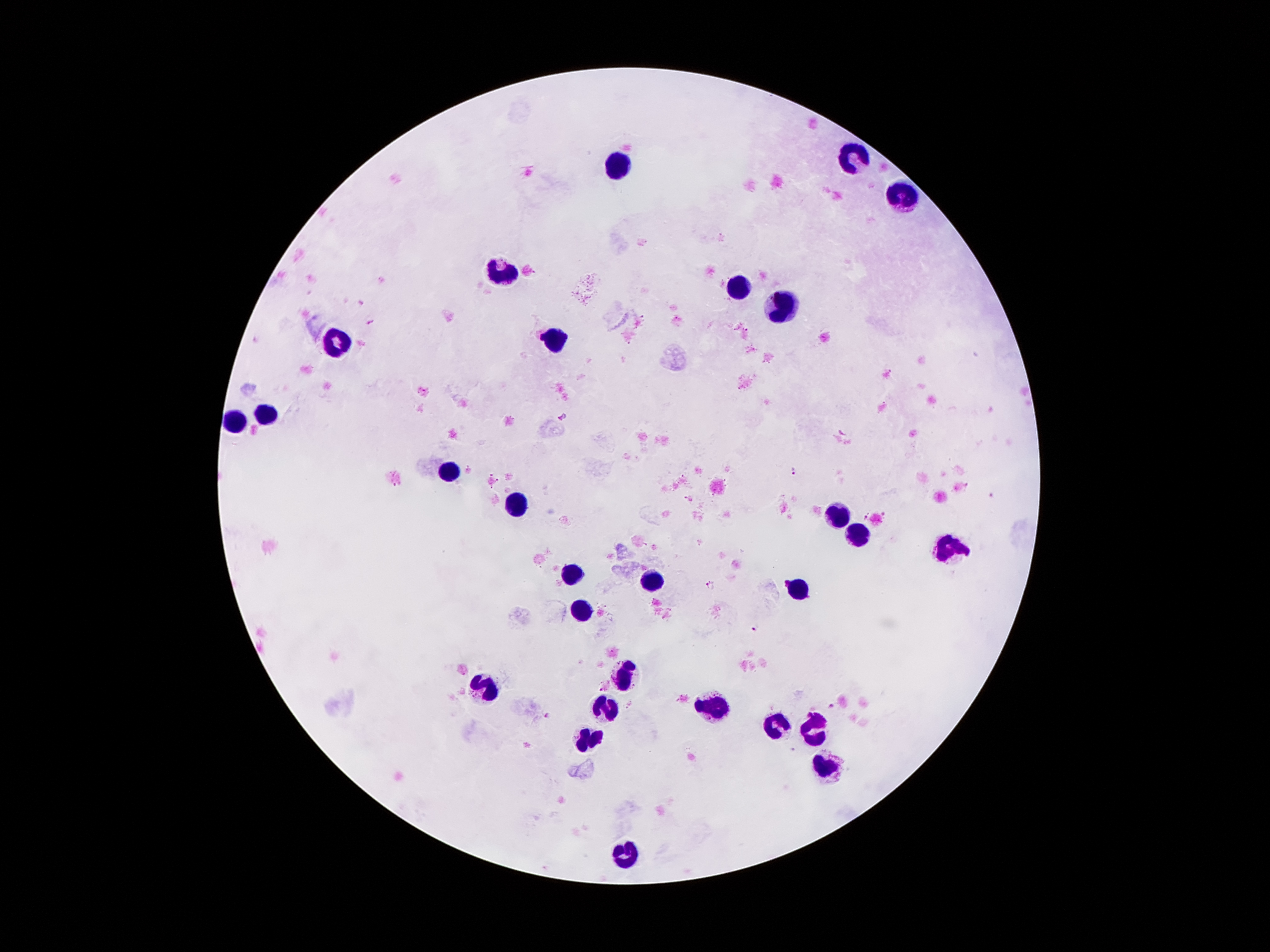

Approximate object centers, in pixels from the top-left corner. Leukocyte locations: (x=853, y=158), (x=618, y=162), (x=902, y=197), (x=501, y=272), (x=741, y=287), (x=784, y=308), (x=554, y=342), (x=337, y=344), (x=265, y=414), (x=236, y=422), (x=450, y=472), (x=511, y=504), (x=835, y=518), (x=859, y=537), (x=952, y=550), (x=570, y=571), (x=652, y=579), (x=798, y=591), (x=583, y=610), (x=624, y=675), (x=484, y=688), (x=603, y=703), (x=712, y=708), (x=820, y=726), (x=777, y=727), (x=589, y=739), (x=827, y=768), (x=626, y=854). Plasmodium parasite locations: (x=563, y=415), (x=793, y=470), (x=867, y=515), (x=711, y=583), (x=754, y=627), (x=834, y=706), (x=547, y=715). Image is 1270×952 pixels. Patient malaria status: infected with Plasmodium falciparum. Giemsa-stained preparation. 100x magnification. Thick blood smear. Smartphone photograph taken through the microscope eyepiece. One field from this slide.